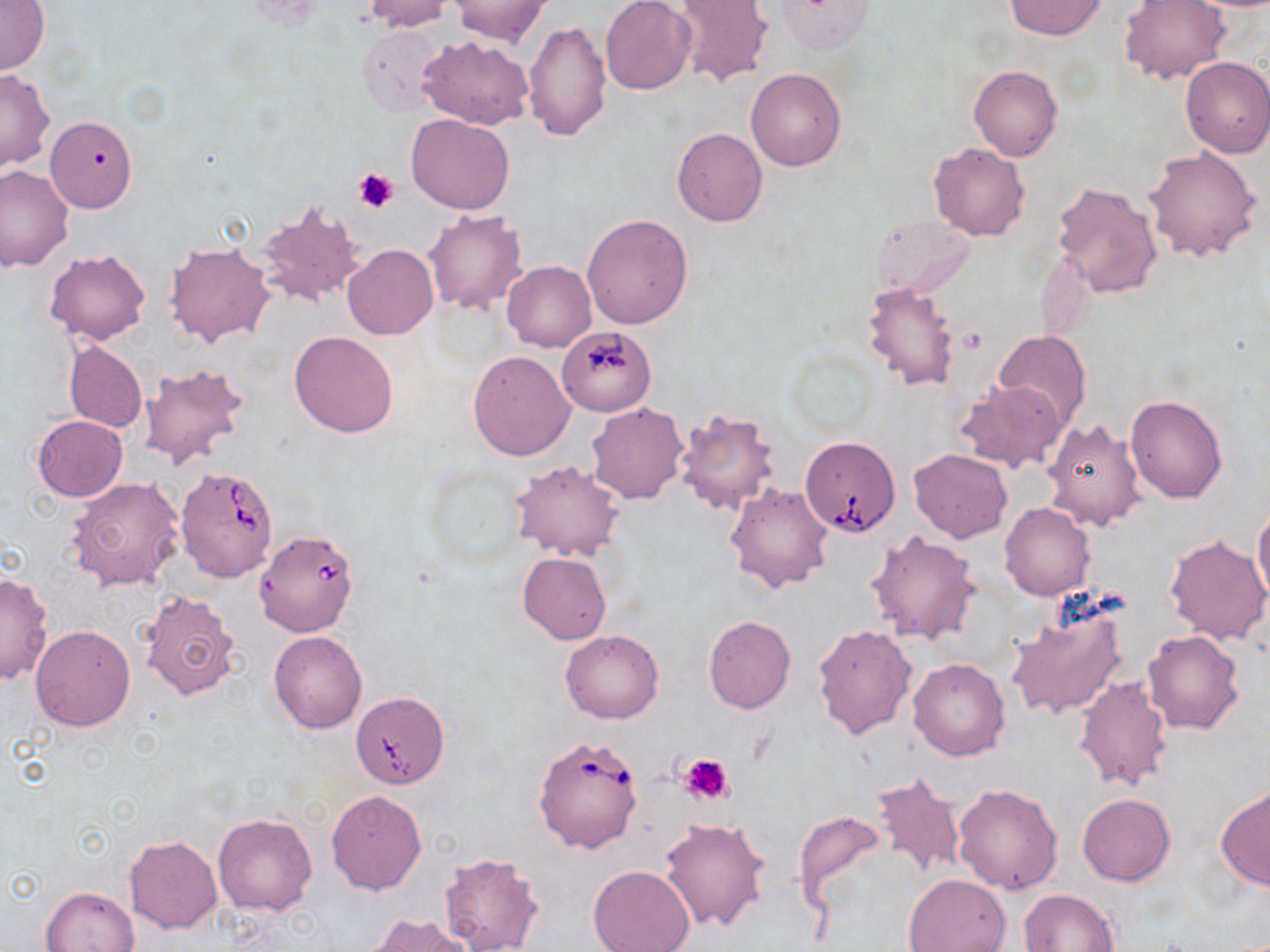
slide-level diagnosis = Babesia divergens
modality = optical microscopy
magnification = 1000x
image size = 1270×952 pixels
uninfected red blood cell locations = approximate bounding boxes as [x1, y1, x2, y2] in pixels: [363, 0, 452, 32], [1003, 0, 1108, 41], [1120, 0, 1228, 86], [1, 1, 49, 76], [450, 1, 549, 46], [601, 1, 695, 95], [671, 1, 773, 87], [775, 1, 877, 55], [523, 21, 612, 144], [357, 24, 447, 117], [418, 35, 533, 130], [1179, 56, 1270, 158], [968, 65, 1062, 161], [746, 67, 847, 171], [0, 70, 55, 172], [406, 113, 516, 214], [38, 119, 130, 216], [672, 127, 767, 227], [929, 143, 1029, 242], [1143, 146, 1262, 263], [0, 165, 74, 271], [1051, 182, 1162, 298], [254, 199, 367, 310], [422, 209, 527, 316], [582, 214, 693, 328], [164, 242, 273, 348], [342, 243, 438, 339], [44, 249, 151, 345], [502, 261, 595, 351], [861, 281, 961, 391], [289, 331, 399, 439], [994, 331, 1092, 428], [63, 340, 147, 433], [467, 351, 575, 461], [138, 364, 249, 471], [955, 378, 1067, 474], [1125, 393, 1227, 503], [587, 403, 687, 505], [674, 410, 780, 516], [32, 415, 128, 501], [1042, 418, 1146, 532], [908, 448, 1012, 543], [510, 461, 624, 562], [66, 477, 186, 592], [725, 482, 834, 593], [1253, 501, 1270, 608], [999, 503, 1095, 600], [867, 530, 981, 643], [1165, 535, 1270, 646], [517, 553, 612, 644], [0, 572, 54, 685], [141, 590, 241, 701], [1006, 601, 1129, 722], [703, 615, 796, 713], [813, 624, 916, 739], [31, 625, 135, 731], [560, 629, 664, 723], [268, 630, 368, 734], [1141, 630, 1246, 735], [908, 658, 1010, 761], [1074, 675, 1174, 791], [346, 690, 449, 795], [870, 772, 965, 881], [953, 782, 1064, 893], [1216, 788, 1270, 890], [326, 790, 427, 894], [1077, 794, 1175, 886], [792, 809, 889, 918], [214, 812, 317, 916], [658, 816, 770, 933], [124, 836, 222, 933], [437, 851, 544, 952], [588, 865, 695, 952], [903, 874, 1012, 952], [41, 885, 138, 951], [1020, 889, 1119, 951], [367, 914, 473, 952]
preparation = thin blood smear
field of view = one of a larger specimen
stain = May-Grünwald-Giemsa
platelet locations = approximate bounding boxes as [x1, y1, x2, y2] in pixels: [353, 166, 399, 212], [678, 753, 734, 805]
Babesia divergens-infected red blood cell locations = approximate bounding boxes as [x1, y1, x2, y2] in pixels: [557, 325, 655, 415], [800, 435, 900, 536], [175, 465, 280, 583], [253, 529, 359, 637], [533, 734, 644, 854]